Assess the morphology of the red blood cells.
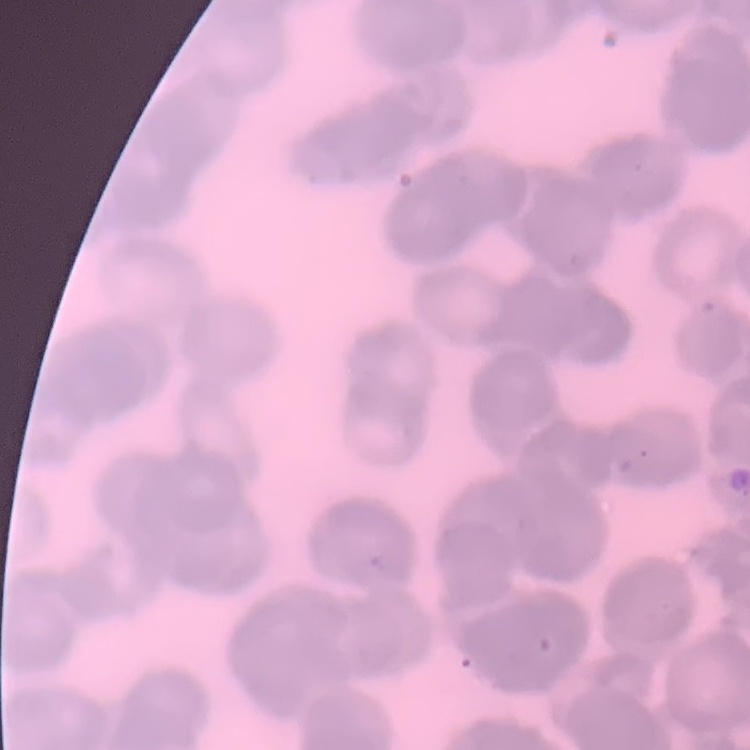
They show rouleaux formation.

preparation = thin blood film
image type = square crop of a larger photomicrograph
stain = Field's or Giemsa